Classify this cell by malaria status.
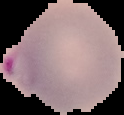

It is parasitized.

Cell region segmented out of the field of view; the surrounding area is masked to black. From a thin blood smear. Image is 124×115 pixels.